Assess this cell for malaria.
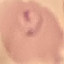
It is parasitized.

Automatically extracted cell patch, resized to 64 × 64 pixels. Photographed with a smartphone camera at the microscope eyepiece. Giemsa-stained preparation. Thin smear of blood.